Name the parasite shown.
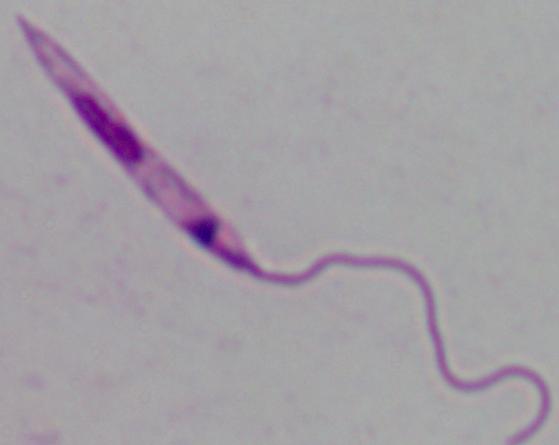
Leishmania.

modality = micrograph
magnification = 1000x